Locate every Plasmodium parasite.
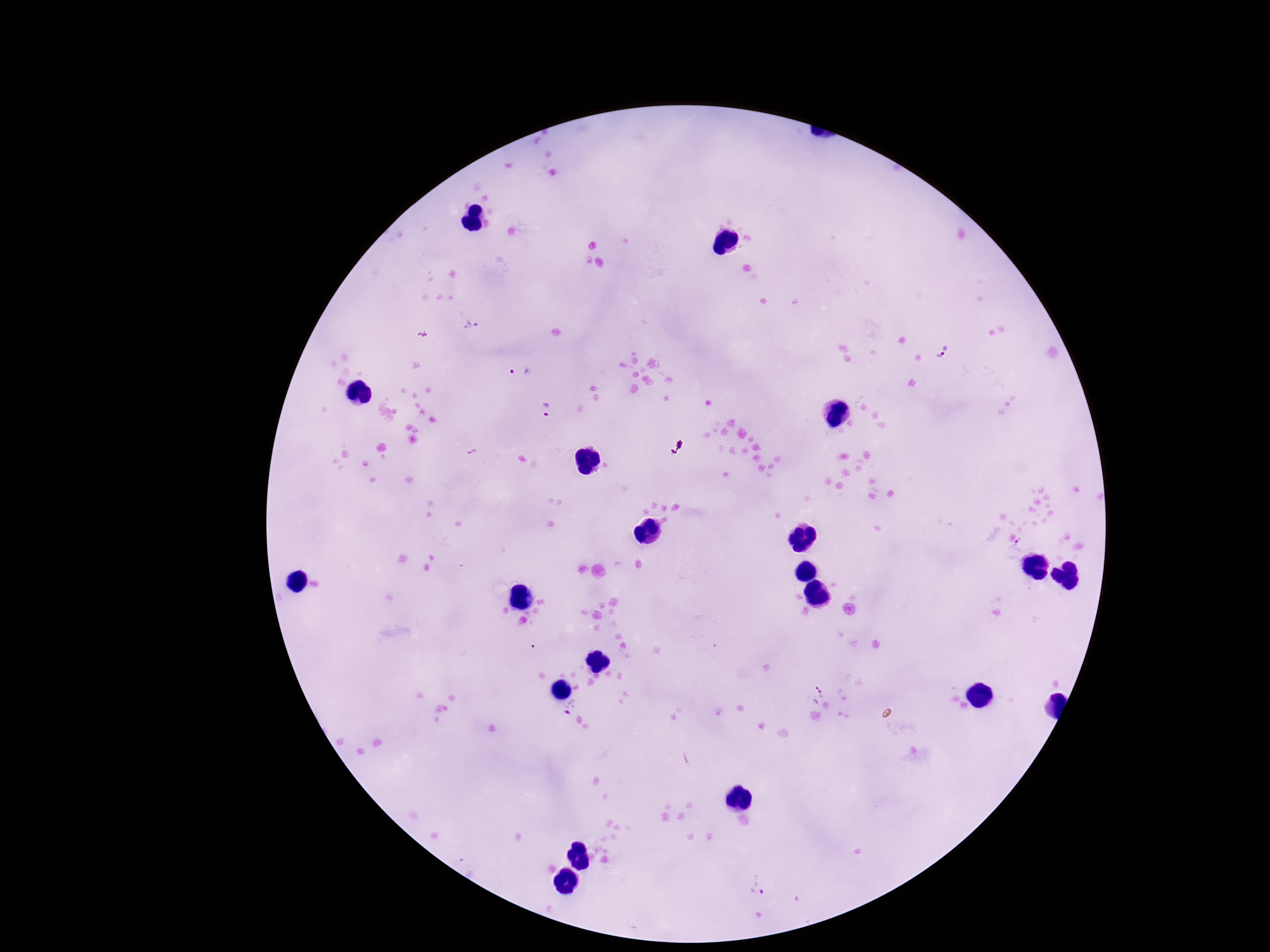
Approximate centers as {x, y} in pixels.
Plasmodium parasites: {470, 326}, {943, 354}, {521, 370}, {547, 410}, {1018, 545}, {815, 691}, {568, 705}, {757, 883}.

field of view = single
preparation = thick blood smear
capture = smartphone camera through the microscope eyepiece
magnification = 100x
stain = Giemsa
image size = 1270×952 pixels
patient malaria status = positive